Classify this cell by malaria status.
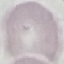
It is uninfected.

stain = Giemsa
preparation = thin smear
image type = automatically extracted cell patch, resized to 64 × 64 pixels
capture = smartphone through the microscope eyepiece